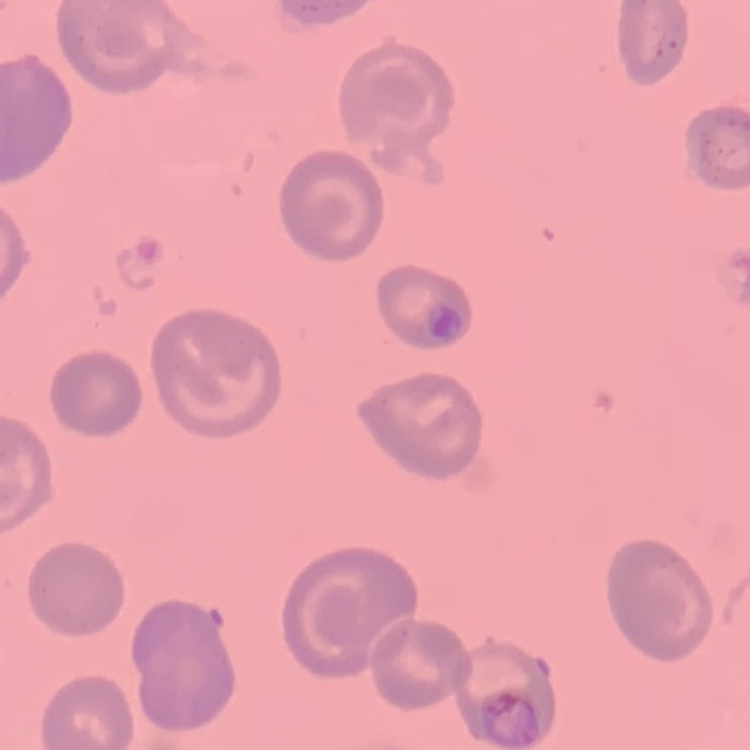 The red blood cells show no rouleaux formation. Thin peripheral smear. Field's or Giemsa stain. One tile cut from a larger photomicrograph.